Identify the parasite.
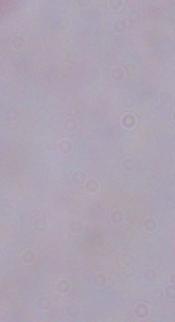

This is a trypanosome.

{
  "modality": "photomicrograph",
  "magnification": "1000x"
}